Report the malaria status of this cell.
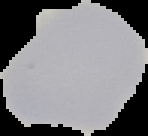

Uninfected.

From a thin blood smear. Segmented cell region on a black background. Image is 148×136 pixels.